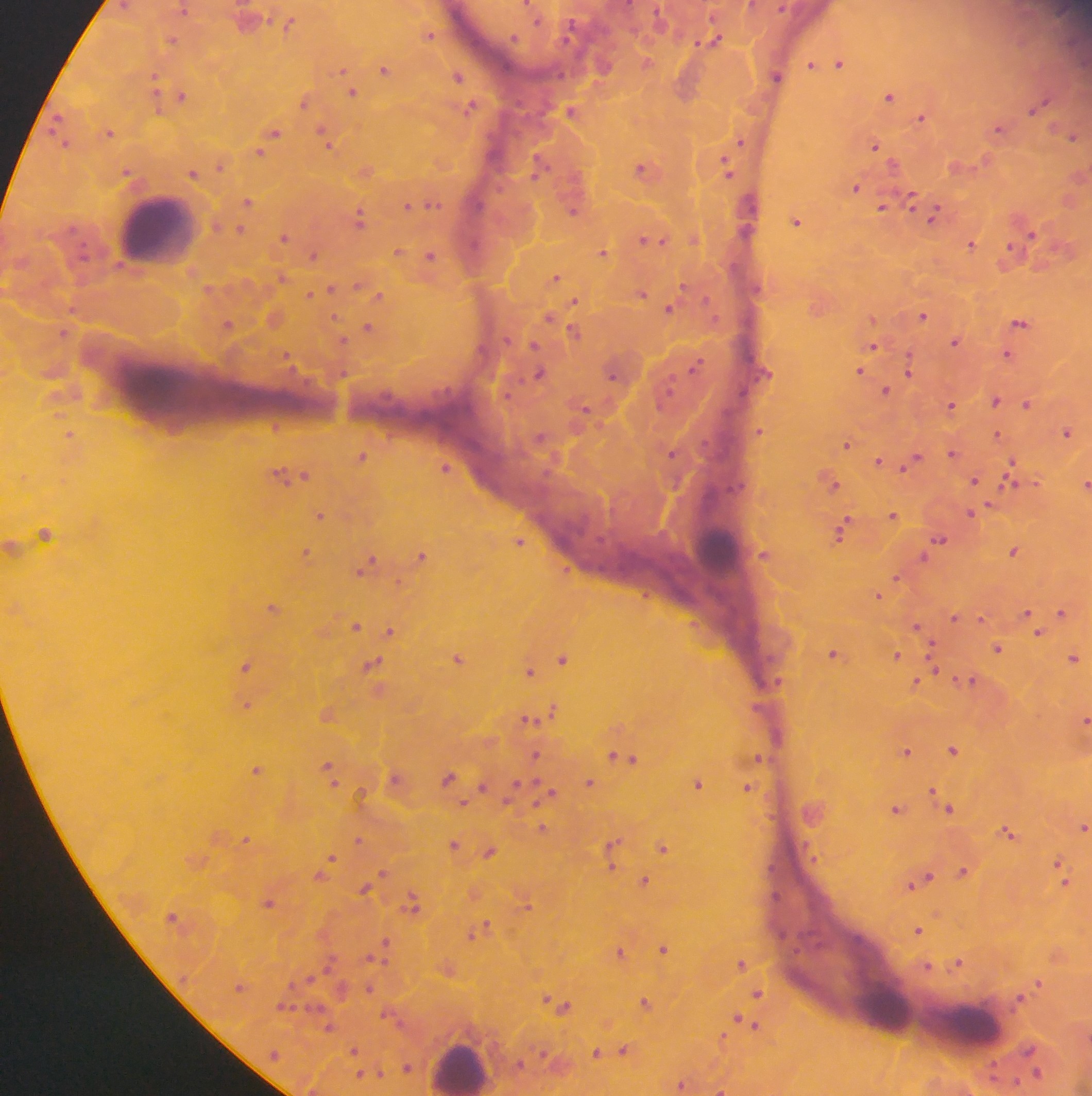

Approximate centers as (x, y) in pixels. Plasmodium parasite locations: (124, 6), (184, 10), (289, 24), (430, 35), (515, 37), (172, 40), (713, 40), (647, 62), (840, 63), (813, 65), (385, 69), (458, 76), (776, 77), (155, 79), (353, 92), (183, 95), (889, 96), (305, 101), (1039, 105), (470, 108), (572, 110), (922, 118), (57, 122), (998, 129), (275, 131), (109, 132), (1073, 137), (327, 139), (742, 141), (64, 144), (876, 145), (260, 152), (540, 164), (220, 166), (728, 167), (643, 168), (366, 171), (128, 172), (193, 172), (856, 187), (912, 199), (247, 201), (432, 204), (408, 206), (884, 206), (573, 210), (934, 215), (359, 218), (797, 222), (241, 229), (1032, 233), (285, 237), (695, 239), (650, 241), (972, 243), (398, 252), (602, 253), (313, 254), (1009, 254), (432, 255), (556, 276), (282, 277), (331, 288), (210, 289), (642, 294), (310, 295), (380, 296), (575, 301), (669, 308), (923, 316), (335, 318), (551, 319), (1020, 323), (229, 324), (368, 328), (63, 331), (576, 331), (343, 341), (955, 342), (874, 346), (1007, 354), (288, 359), (695, 366), (910, 369), (859, 371), (540, 373), (613, 375), (886, 391), (996, 400), (952, 404), (1027, 404), (585, 410), (276, 426), (760, 431), (1067, 431), (70, 434), (997, 435), (846, 444), (673, 453), (953, 453), (362, 456), (879, 462), (912, 463), (1013, 464), (446, 467), (1011, 473), (293, 474), (831, 481), (974, 481), (1085, 483), (974, 512), (892, 514), (321, 515), (842, 530), (44, 533), (940, 540), (519, 541), (1014, 551), (307, 553), (765, 555), (422, 556), (925, 556), (366, 566), (896, 578), (878, 595), (273, 608), (1062, 612), (1029, 615), (955, 617), (356, 625), (918, 628), (390, 631), (1037, 631), (998, 648), (835, 655), (897, 655), (1075, 658), (459, 659), (563, 659), (372, 665), (247, 666), (934, 668), (530, 672), (971, 681), (917, 682), (246, 705), (553, 709), (328, 714), (530, 719), (1085, 720), (954, 750), (907, 751), (537, 754), (759, 758), (628, 759), (256, 770), (330, 770), (396, 777), (449, 778), (589, 783), (699, 784), (748, 787), (483, 788), (548, 793), (362, 795), (936, 795), (946, 803), (463, 804), (897, 809), (1083, 826), (542, 828), (1009, 832), (246, 839), (358, 840), (454, 844), (612, 847), (663, 848), (490, 852), (331, 857), (1060, 863), (384, 872), (963, 872), (323, 873), (1064, 878), (645, 881), (921, 881), (365, 889), (269, 902), (412, 904), (526, 904), (482, 929), (919, 930), (475, 933), (385, 944), (664, 948), (620, 952), (959, 962), (741, 963), (929, 967), (449, 970), (1039, 982), (369, 988), (758, 993), (646, 1003), (562, 1006), (388, 1014), (747, 1023), (329, 1027), (723, 1038), (354, 1051), (625, 1051), (597, 1052), (1032, 1061), (358, 1062), (407, 1067), (1036, 1072), (380, 1073), (370, 1074), (361, 1075), (682, 1084), (722, 1089). Leukocyte locations: (156, 230), (717, 546), (885, 1008), (971, 1027), (460, 1066). Image is 1092×1096 pixels. Sample from Ghana. Thick blood film. Photographed through a microscope with a mobile-phone camera. Single field of view.